Comment on the morphology of the erythrocytes.
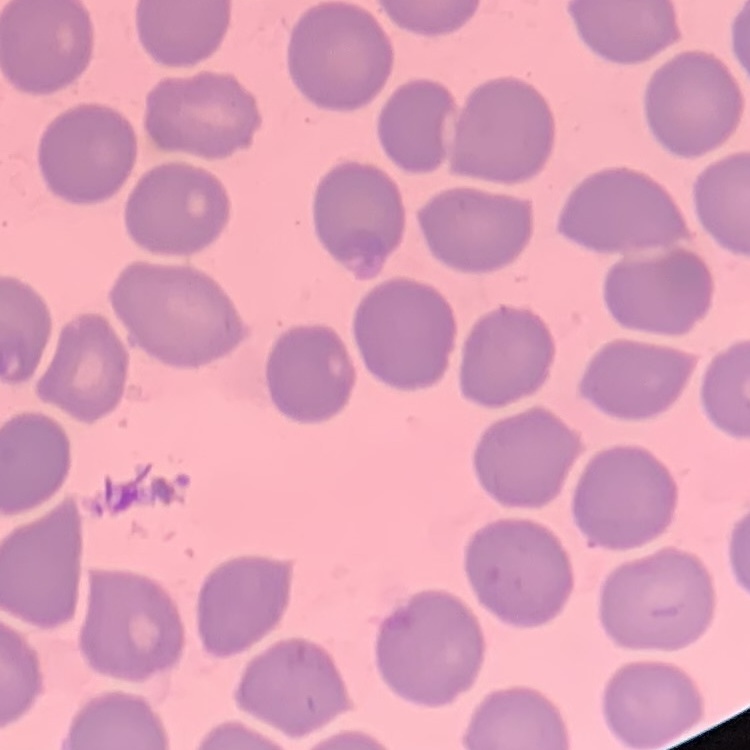

They show no rouleaux formation.

Square crop of a larger photomicrograph. Thin blood film. Stained with either Field's or Giemsa.